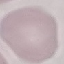
Summary:
  - Result: no malaria parasites seen
  - Stain: Giemsa
  - Capture: smartphone through the microscope eyepiece
  - Image type: cell patch, automatically extracted from a larger field of view and resized to 64 × 64 pixels
  - Preparation: thin smear